Give the preparation type.
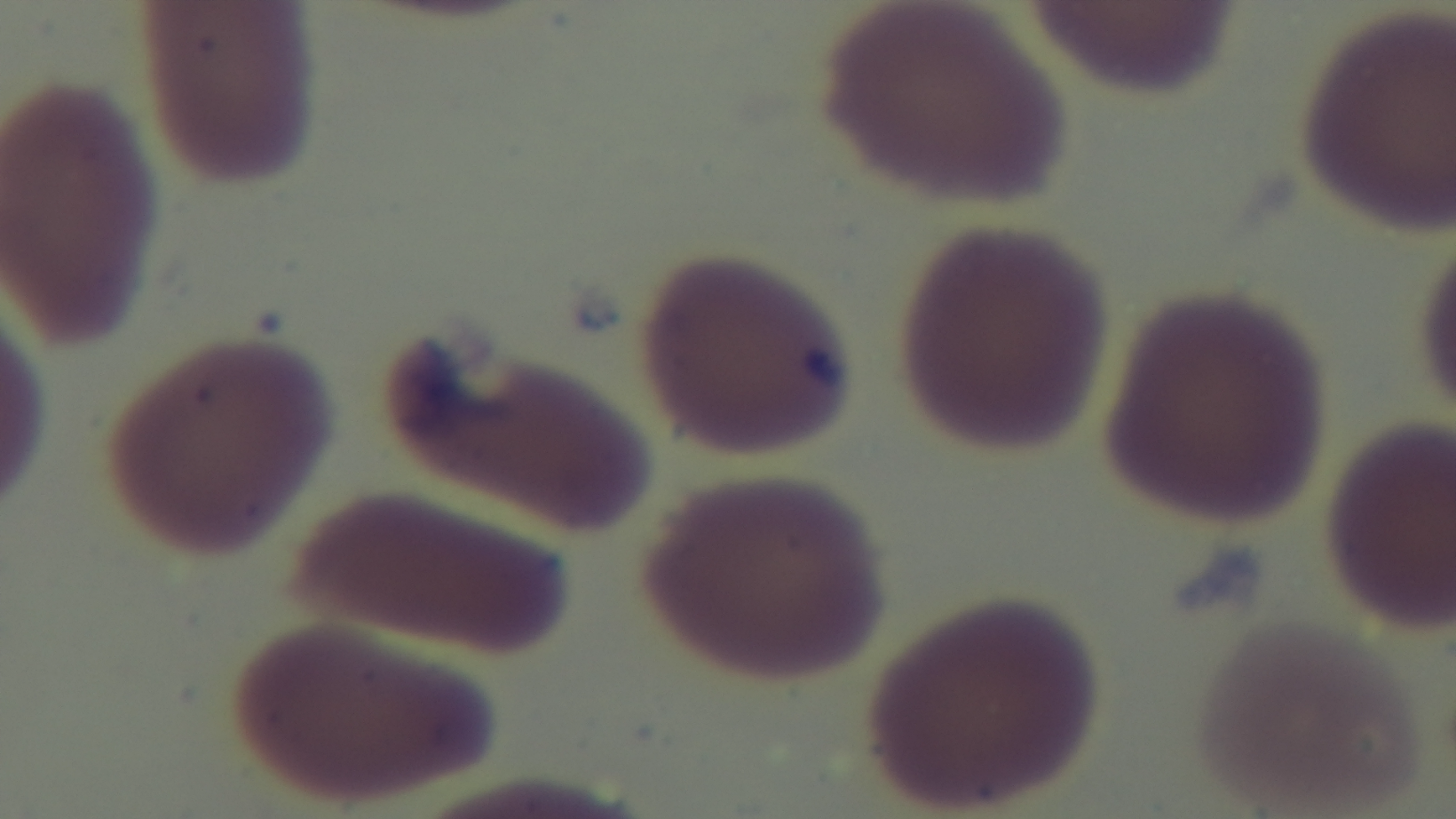
It is a thin blood film.

Summary:
  - Objective: 100x oil immersion
  - Stain: Giemsa
  - Modality: light microscopy
  - Malaria status: uninfected
  - Capture: mounted 4K digital camera
  - Field of view: single